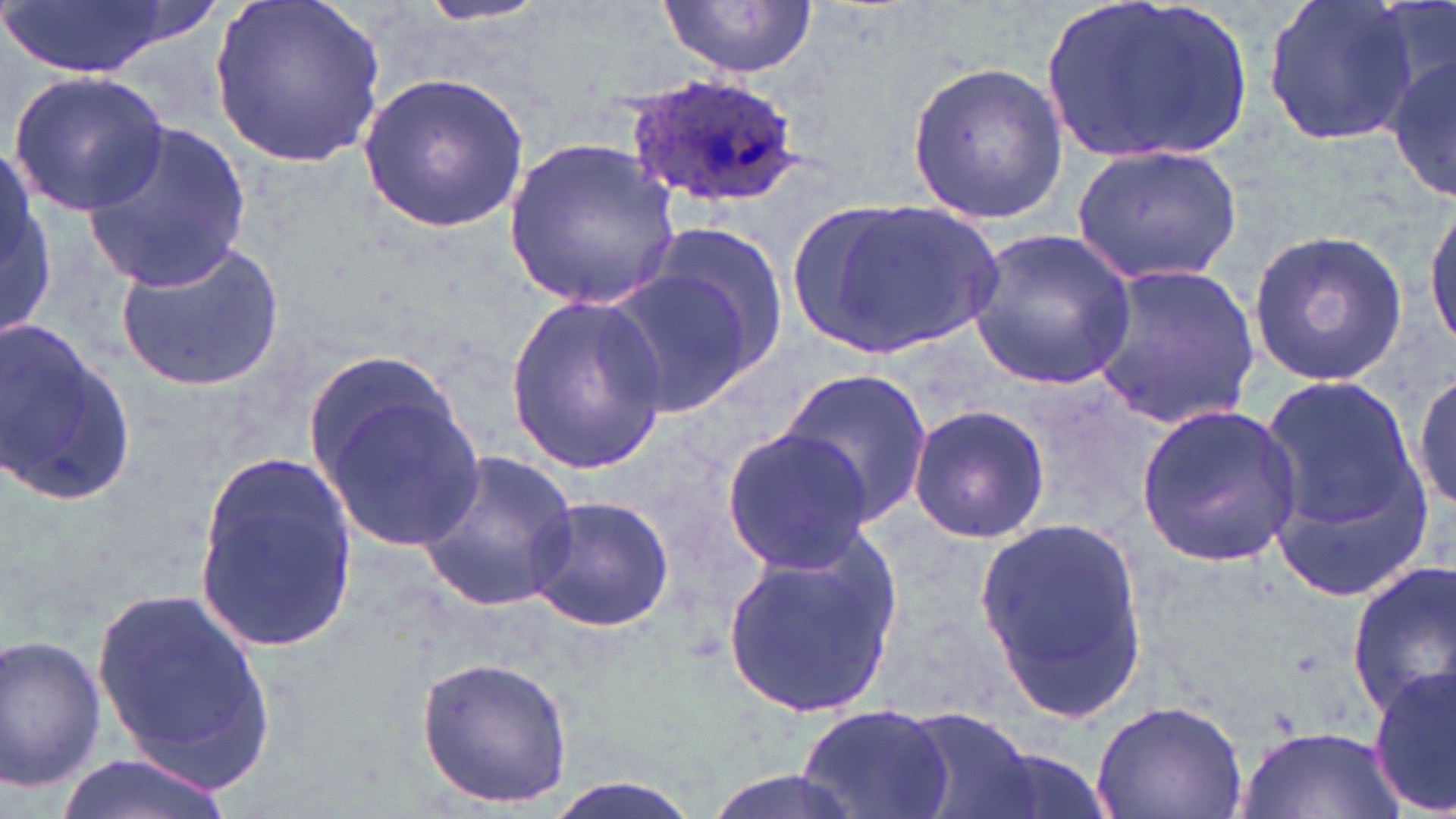

Summary:
  - Coordinate format: approximate bounding boxes as named x1/y1/x2/y2 corners in pixels
  - Plasmodium ovale-infected red blood cell locations: (x1=625, y1=74, x2=807, y2=210)
  - Uninfected red blood cell locations: (x1=0, y1=0, x2=188, y2=78), (x1=211, y1=0, x2=387, y2=165), (x1=413, y1=0, x2=557, y2=28), (x1=657, y1=0, x2=818, y2=80), (x1=1044, y1=0, x2=1258, y2=166), (x1=1260, y1=0, x2=1422, y2=148), (x1=1387, y1=47, x2=1456, y2=207), (x1=906, y1=58, x2=1067, y2=224), (x1=359, y1=71, x2=532, y2=231), (x1=9, y1=72, x2=170, y2=216), (x1=82, y1=123, x2=253, y2=290), (x1=506, y1=136, x2=681, y2=305), (x1=1071, y1=143, x2=1241, y2=287), (x1=1, y1=151, x2=54, y2=340), (x1=788, y1=194, x2=1005, y2=362), (x1=1425, y1=202, x2=1456, y2=350), (x1=647, y1=220, x2=791, y2=373), (x1=1246, y1=227, x2=1409, y2=385), (x1=966, y1=229, x2=1140, y2=388), (x1=114, y1=240, x2=284, y2=390), (x1=1088, y1=261, x2=1260, y2=430), (x1=605, y1=270, x2=753, y2=418), (x1=506, y1=293, x2=667, y2=473), (x1=0, y1=316, x2=135, y2=511), (x1=774, y1=368, x2=933, y2=526), (x1=1410, y1=368, x2=1456, y2=513), (x1=1257, y1=370, x2=1434, y2=587), (x1=316, y1=381, x2=484, y2=556), (x1=906, y1=402, x2=1051, y2=545), (x1=1134, y1=402, x2=1299, y2=564), (x1=721, y1=427, x2=876, y2=571), (x1=414, y1=449, x2=581, y2=612), (x1=194, y1=451, x2=362, y2=648), (x1=525, y1=494, x2=675, y2=633), (x1=975, y1=515, x2=1148, y2=715), (x1=720, y1=535, x2=902, y2=717), (x1=1346, y1=563, x2=1456, y2=722), (x1=89, y1=581, x2=279, y2=788), (x1=0, y1=633, x2=107, y2=794), (x1=416, y1=655, x2=575, y2=810), (x1=1370, y1=671, x2=1456, y2=811), (x1=1091, y1=698, x2=1248, y2=819), (x1=798, y1=703, x2=955, y2=819), (x1=903, y1=709, x2=1038, y2=819), (x1=1236, y1=724, x2=1403, y2=819), (x1=960, y1=744, x2=1117, y2=819), (x1=55, y1=752, x2=238, y2=819), (x1=695, y1=769, x2=876, y2=819), (x1=533, y1=774, x2=711, y2=819)
  - Slide-level diagnosis: Plasmodium ovale
  - Preparation: thin blood film
  - Field of view: single
  - Modality: light microscopy
  - Magnification: 1000x
  - Image size: 1456×819 pixels
  - Stain: May-Grünwald-Giemsa